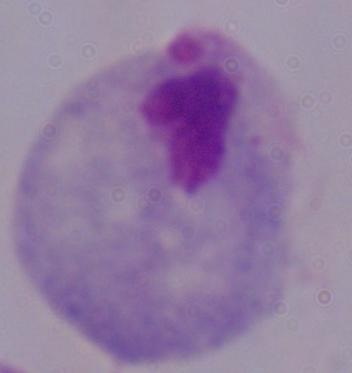
Captured at 1000x magnification. Photomicrograph. A trichomonad is shown.